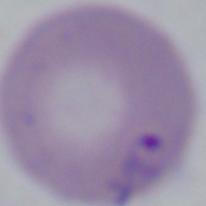

Summary:
  - Identification: Babesia
  - Modality: micrograph
  - Magnification: 1000x